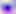

Captured at 400x magnification. Micrograph. Toxoplasma gondii is seen.